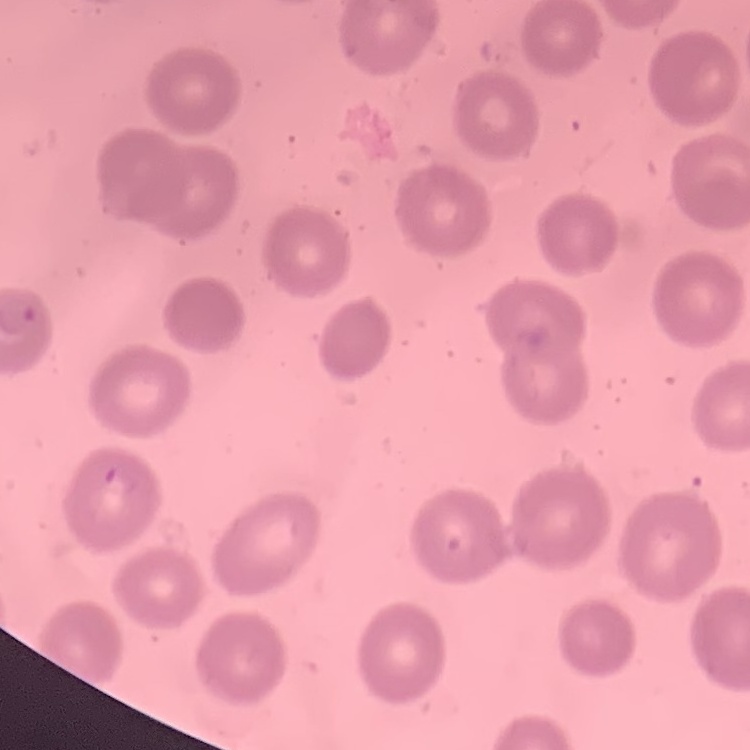

The erythrocytes show no rouleaux formation. Stained with either Field's or Giemsa. One tile cut from a larger photomicrograph. Thin peripheral smear.